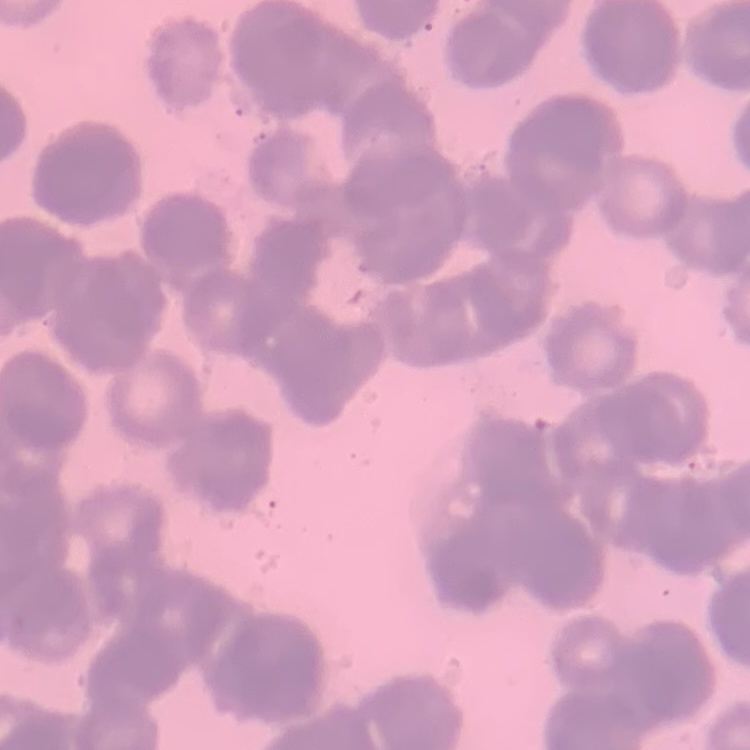

Summary:
  - Red blood cell morphology: rouleaux formation
  - Preparation: thin blood film
  - Stain: Field's or Giemsa
  - Image type: square crop of a larger photomicrograph